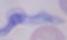
A trypanosome is shown. Micrograph. 1000x magnification.